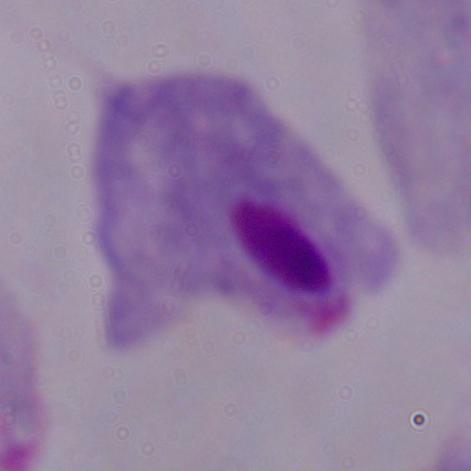
Captured at 1000x magnification. A trichomonad is shown. Photomicrograph.